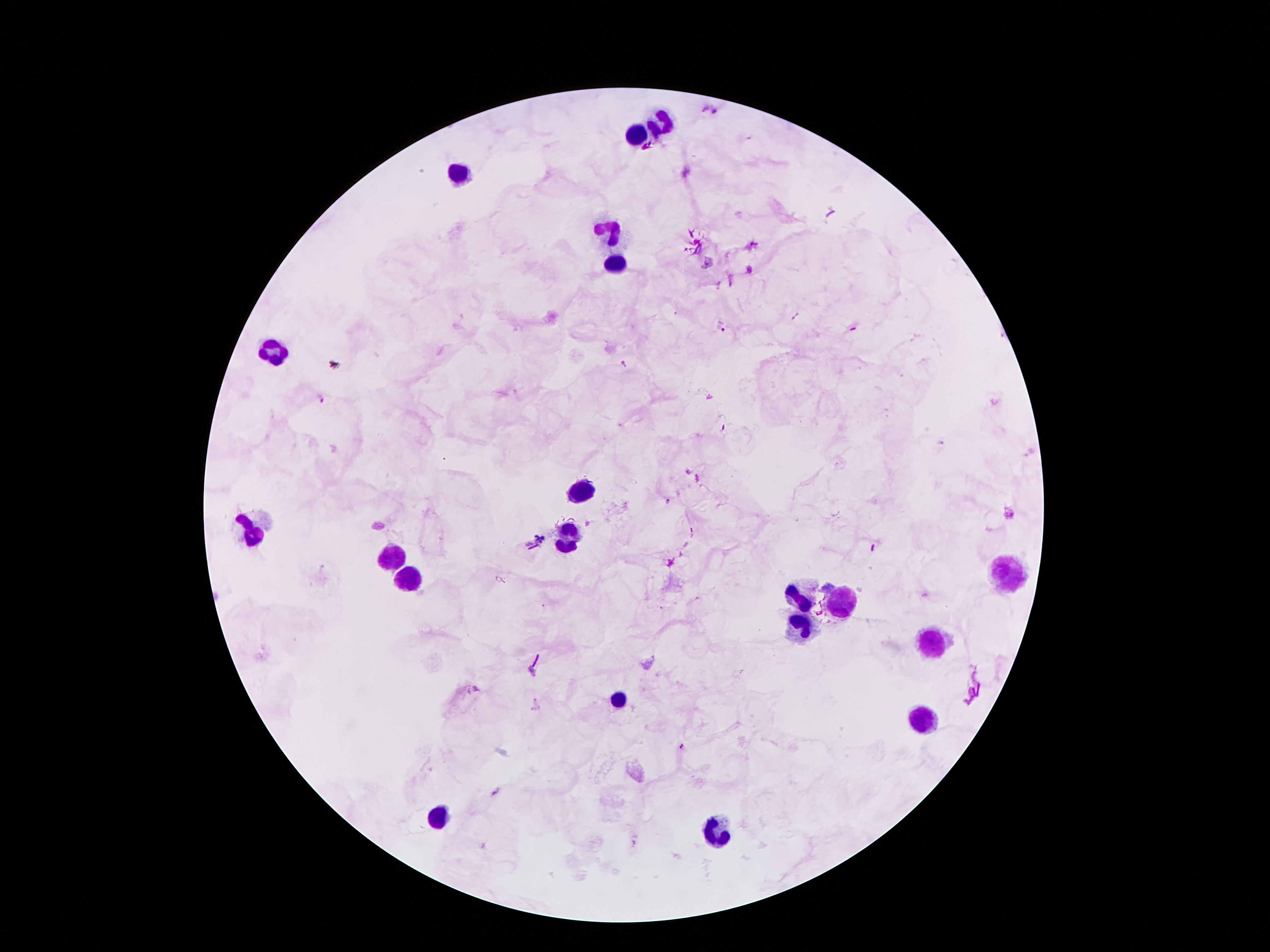
Approximate centers as (x, y) in pixels.
Summary:
  - Malaria parasite locations: (721, 326), (623, 365), (320, 398), (668, 502), (1011, 515), (541, 536), (474, 690), (684, 747)
  - Leukocyte locations: (664, 124), (639, 136), (463, 171), (615, 232), (613, 265), (275, 351), (584, 492), (248, 529), (567, 542), (395, 561), (1003, 573), (411, 576), (844, 596), (804, 599), (796, 626), (930, 647), (617, 699), (922, 720), (437, 821), (716, 827)
  - Patient malaria status: positive for Plasmodium falciparum
  - Field of view: one from this slide
  - Preparation: thick blood smear
  - Magnification: 100x
  - Stain: Giemsa
  - Image size: 1270×952 pixels
  - Capture: smartphone through the microscope eyepiece